Identify the blood parasite species.
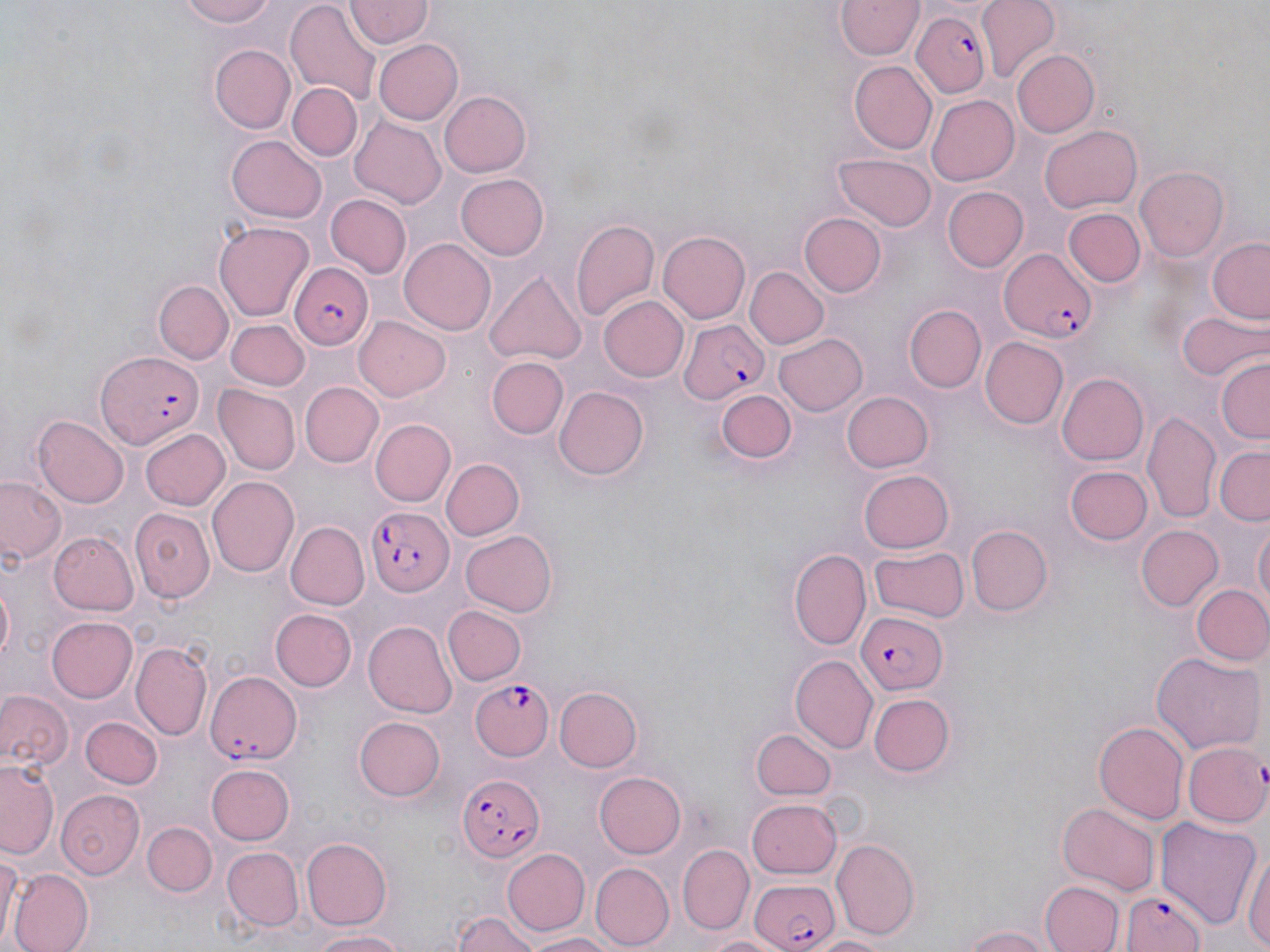
Plasmodium falciparum.

Summary:
  - Coordinate format: approximate bounding boxes as (x1, y1, x2, y2) in pixels
  - Plasmodium falciparum-infected red blood cell locations: (911, 11, 993, 101), (997, 247, 1100, 343), (286, 263, 371, 348), (678, 318, 772, 401), (97, 350, 206, 446), (365, 506, 451, 598), (854, 609, 946, 693), (204, 668, 302, 765), (472, 678, 557, 756), (1186, 741, 1270, 828), (460, 772, 547, 864), (746, 877, 842, 951), (1119, 888, 1210, 952)
  - Uninfected red blood cell locations: (173, 0, 286, 27), (836, 1, 922, 61), (978, 1, 1063, 83), (344, 2, 432, 49), (287, 4, 381, 103), (374, 38, 463, 124), (210, 44, 296, 133), (1010, 49, 1098, 137), (850, 60, 938, 154), (287, 83, 362, 160), (439, 89, 531, 177), (926, 94, 1020, 186), (349, 117, 446, 207), (1039, 125, 1141, 215), (229, 134, 326, 220), (835, 153, 935, 231), (1135, 167, 1229, 262), (455, 173, 549, 259), (945, 186, 1028, 272), (328, 195, 412, 279), (1062, 208, 1145, 288), (802, 213, 887, 296), (569, 215, 659, 324), (215, 219, 312, 318), (658, 231, 750, 324), (400, 237, 496, 335), (1207, 238, 1270, 324), (745, 266, 828, 349), (485, 268, 585, 363), (155, 281, 230, 364), (598, 295, 687, 382), (903, 305, 986, 390), (1174, 309, 1265, 384), (355, 315, 452, 402), (227, 320, 307, 390), (773, 333, 865, 415), (979, 337, 1068, 429), (1214, 354, 1270, 447), (488, 357, 568, 440), (1056, 373, 1149, 466), (299, 381, 384, 468), (216, 385, 299, 473), (554, 385, 649, 481), (715, 388, 796, 463), (842, 389, 932, 472), (1144, 411, 1222, 525), (32, 416, 128, 506), (371, 417, 455, 506), (139, 428, 228, 510), (1215, 446, 1270, 525), (440, 457, 524, 541), (1064, 466, 1153, 545), (858, 470, 955, 553), (209, 474, 300, 578), (0, 476, 64, 568), (131, 507, 215, 602), (1251, 519, 1269, 617), (284, 521, 367, 610), (964, 524, 1052, 614), (1135, 524, 1224, 611), (460, 529, 559, 617), (49, 530, 137, 615), (869, 547, 967, 624), (789, 549, 872, 651), (0, 576, 15, 674), (1191, 584, 1270, 666), (441, 605, 526, 685), (269, 609, 356, 693), (45, 616, 137, 703), (363, 619, 456, 716), (132, 641, 211, 743), (1152, 651, 1266, 756), (790, 654, 878, 755), (553, 686, 642, 773), (0, 687, 73, 774), (869, 692, 955, 777), (81, 714, 160, 789), (354, 714, 447, 801), (1094, 720, 1190, 822), (753, 729, 835, 800), (1, 758, 61, 861), (205, 764, 295, 845), (595, 770, 686, 858), (58, 790, 146, 877), (748, 797, 841, 877), (1056, 802, 1159, 894), (1157, 817, 1263, 928), (144, 822, 217, 897), (300, 836, 393, 929), (831, 840, 921, 937), (1243, 844, 1269, 952), (0, 845, 19, 952), (678, 845, 755, 931), (221, 846, 302, 931), (501, 846, 589, 936), (590, 862, 672, 949), (7, 869, 92, 952), (1041, 879, 1125, 952), (450, 911, 541, 952), (963, 924, 1053, 952), (308, 929, 412, 950), (519, 931, 619, 950), (699, 932, 788, 951), (810, 935, 888, 952)
  - Field of view: single
  - Image size: 1270×952 pixels
  - Magnification: 1000x
  - Modality: optical microscopy
  - Preparation: thin blood smear
  - Stain: May-Grünwald-Giemsa